Identify the blood parasite species.
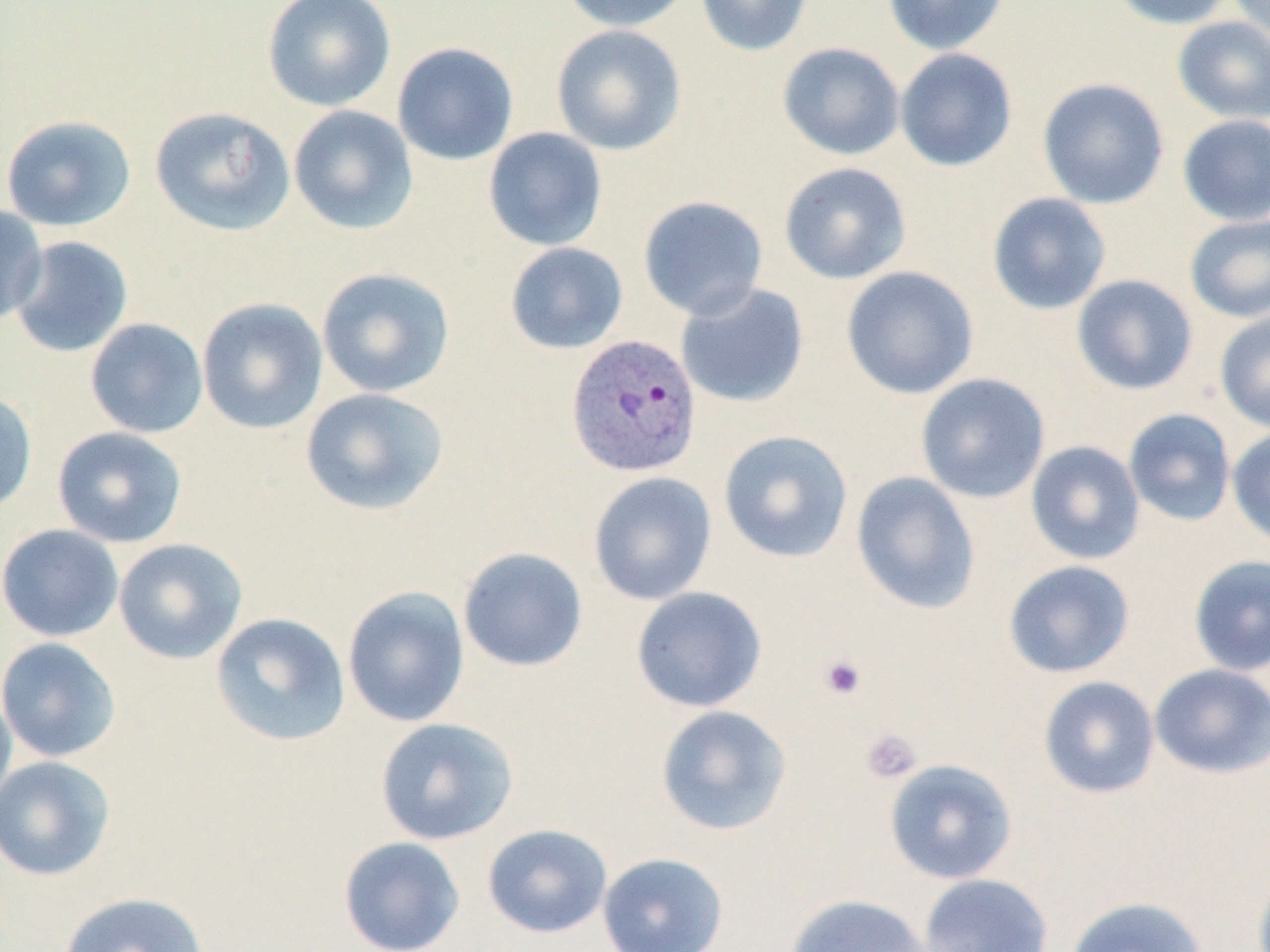

Plasmodium vivax.

Approximate bounding boxes as named x1/y1/x2/y2 corners in pixels. Uninfected red blood cell locations: (x1=262, y1=0, x2=396, y2=112), (x1=560, y1=0, x2=695, y2=32), (x1=695, y1=0, x2=814, y2=56), (x1=882, y1=0, x2=1009, y2=55), (x1=1107, y1=0, x2=1236, y2=30), (x1=1229, y1=0, x2=1270, y2=45), (x1=1172, y1=16, x2=1270, y2=124), (x1=551, y1=24, x2=687, y2=156), (x1=392, y1=42, x2=519, y2=166), (x1=777, y1=42, x2=905, y2=161), (x1=894, y1=48, x2=1018, y2=172), (x1=1037, y1=78, x2=1169, y2=209), (x1=288, y1=105, x2=418, y2=235), (x1=149, y1=106, x2=296, y2=236), (x1=1177, y1=114, x2=1270, y2=226), (x1=0, y1=115, x2=136, y2=232), (x1=483, y1=127, x2=608, y2=251), (x1=779, y1=162, x2=911, y2=285), (x1=987, y1=192, x2=1111, y2=315), (x1=638, y1=195, x2=768, y2=320), (x1=0, y1=204, x2=48, y2=326), (x1=1184, y1=213, x2=1270, y2=323), (x1=8, y1=236, x2=133, y2=358), (x1=504, y1=242, x2=629, y2=354), (x1=841, y1=266, x2=979, y2=400), (x1=316, y1=267, x2=455, y2=398), (x1=1071, y1=274, x2=1198, y2=395), (x1=675, y1=282, x2=810, y2=408), (x1=196, y1=297, x2=329, y2=435), (x1=1214, y1=309, x2=1270, y2=433), (x1=84, y1=318, x2=209, y2=439), (x1=916, y1=373, x2=1050, y2=503), (x1=300, y1=387, x2=449, y2=516), (x1=0, y1=390, x2=38, y2=516), (x1=1123, y1=408, x2=1236, y2=526), (x1=51, y1=426, x2=188, y2=547), (x1=1226, y1=427, x2=1270, y2=549), (x1=718, y1=430, x2=853, y2=563), (x1=1025, y1=440, x2=1145, y2=565), (x1=587, y1=471, x2=717, y2=605), (x1=851, y1=471, x2=981, y2=614), (x1=0, y1=524, x2=123, y2=641), (x1=113, y1=538, x2=248, y2=664), (x1=457, y1=546, x2=589, y2=672), (x1=1188, y1=555, x2=1270, y2=676), (x1=1003, y1=560, x2=1135, y2=678), (x1=343, y1=586, x2=470, y2=727), (x1=631, y1=586, x2=767, y2=712), (x1=209, y1=612, x2=351, y2=746), (x1=0, y1=637, x2=121, y2=763), (x1=1149, y1=663, x2=1270, y2=778), (x1=1038, y1=676, x2=1160, y2=798), (x1=0, y1=682, x2=17, y2=818), (x1=655, y1=705, x2=792, y2=836), (x1=375, y1=717, x2=519, y2=845), (x1=0, y1=755, x2=117, y2=882), (x1=883, y1=759, x2=1017, y2=884), (x1=481, y1=823, x2=613, y2=938), (x1=338, y1=836, x2=466, y2=952), (x1=597, y1=851, x2=730, y2=952), (x1=918, y1=873, x2=1053, y2=952), (x1=59, y1=891, x2=209, y2=952), (x1=784, y1=893, x2=933, y2=952), (x1=1064, y1=896, x2=1209, y2=952). Plasmodium vivax-infected red blood cell locations: (x1=565, y1=334, x2=703, y2=478). Platelet locations: (x1=819, y1=655, x2=866, y2=700), (x1=859, y1=729, x2=922, y2=784). May-Grünwald-Giemsa-stained preparation. 1000x magnification. Single field of view. Image is 1270×952 pixels. Thin blood smear. Optical microscopy.